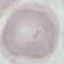
{
  "malaria_status": "uninfected",
  "preparation": "thin smear",
  "stain": "Giemsa",
  "capture": "smartphone camera at the microscope eyepiece",
  "image_type": "cell patch, automatically extracted from a larger field of view and resized to 64 × 64 pixels"
}